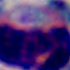
magnification = 1000x
modality = photomicrograph
identification = leukocyte